Give the position of every Plasmodium parasite visible.
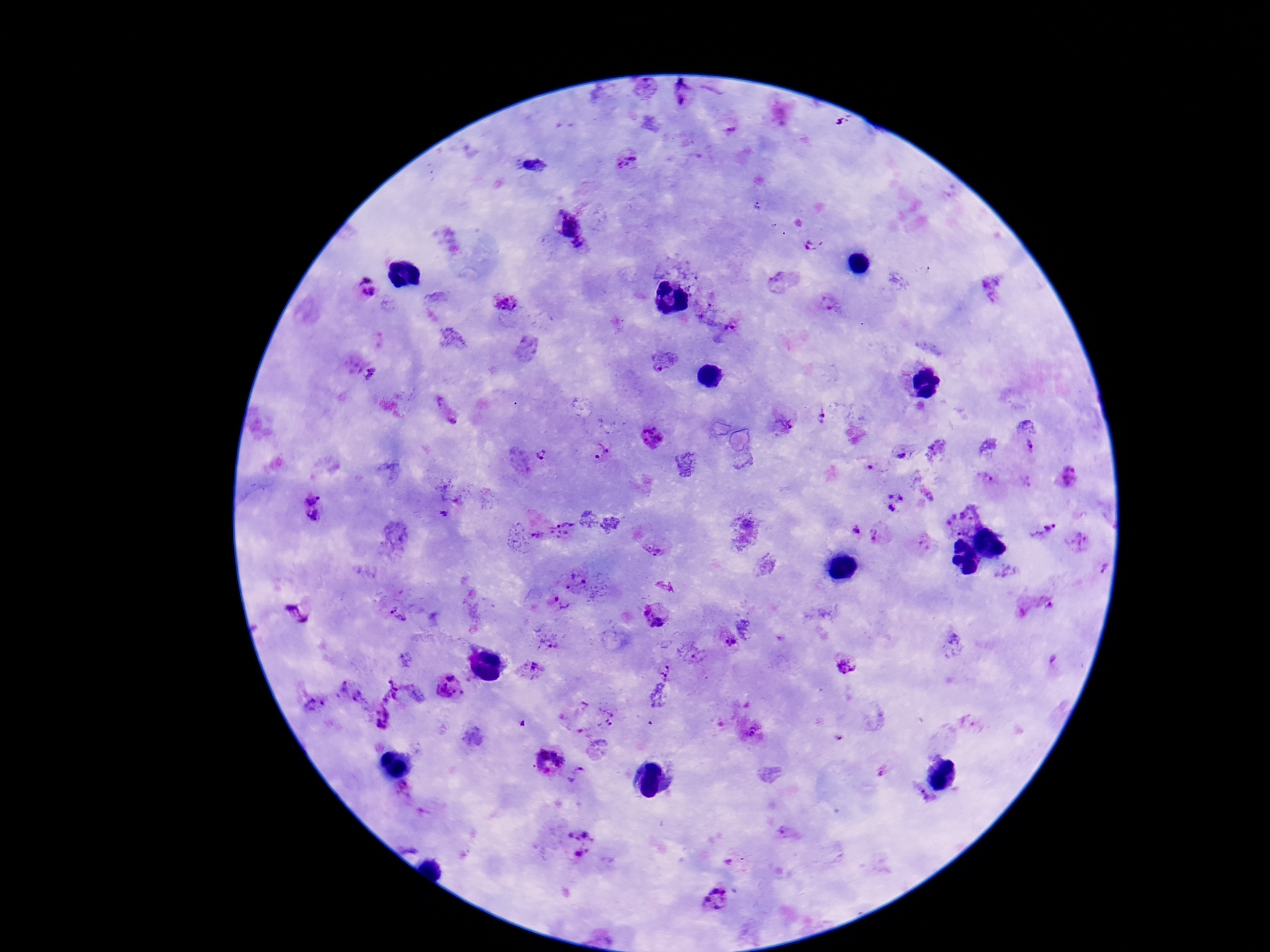

Approximate object centers, in pixels from the top-left corner.
Plasmodium parasites: (x=646, y=89), (x=683, y=99), (x=728, y=128), (x=627, y=162), (x=566, y=224), (x=813, y=245), (x=581, y=248), (x=781, y=280), (x=368, y=288), (x=992, y=291), (x=505, y=301), (x=826, y=303), (x=707, y=311), (x=733, y=326), (x=664, y=361), (x=371, y=377), (x=446, y=412), (x=821, y=416), (x=784, y=422), (x=651, y=438), (x=1032, y=448), (x=600, y=452), (x=899, y=453), (x=541, y=456), (x=1071, y=474), (x=987, y=480), (x=894, y=500), (x=312, y=507), (x=960, y=518), (x=1042, y=528), (x=560, y=529), (x=856, y=530), (x=876, y=535), (x=535, y=536), (x=922, y=543), (x=1080, y=543), (x=650, y=547), (x=1103, y=570), (x=577, y=580), (x=563, y=603), (x=1035, y=605), (x=296, y=614), (x=397, y=614), (x=656, y=614), (x=549, y=637), (x=724, y=641), (x=952, y=644), (x=695, y=655), (x=1055, y=660), (x=845, y=667), (x=532, y=670), (x=667, y=672), (x=448, y=687), (x=390, y=689), (x=348, y=690), (x=418, y=692), (x=312, y=706), (x=380, y=716), (x=597, y=717), (x=969, y=723), (x=751, y=731), (x=548, y=762), (x=579, y=775), (x=403, y=791), (x=924, y=798), (x=788, y=833), (x=578, y=842), (x=728, y=859), (x=718, y=899).

magnification = 100x
patient malaria status = infected
preparation = thick blood smear
capture = smartphone camera through the microscope eyepiece
stain = Giemsa
image size = 1270×952 pixels
field of view = single